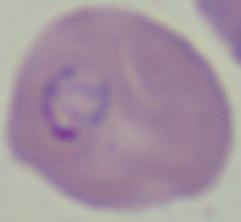

Photomicrograph. A Babesia parasite is seen. 1000x magnification.